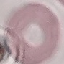
Summary:
  - Malaria status: uninfected
  - Image type: cell patch, automatically extracted from a larger field of view and resized to 64 × 64 pixels
  - Preparation: thin smear
  - Stain: Giemsa
  - Capture: smartphone through the microscope eyepiece